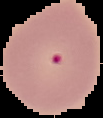

Summary:
  - Preparation: thin blood smear
  - Malaria status: uninfected
  - Image size: 103×118 pixels
  - Image type: cell region segmented out of the field of view; surrounding area masked to black